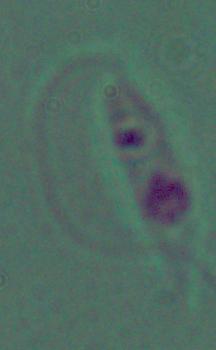
Summary:
  - Magnification: 1000x
  - Modality: photomicrograph
  - Identification: Leishmania